Report the malaria status of this cell.
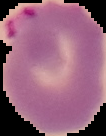

Parasitized.

preparation = thin blood smear
image type = segmented cell region on a black background
image size = 106×136 pixels